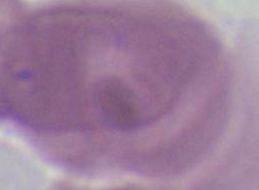

Micrograph. A red blood cell is seen. Captured at 1000x magnification.